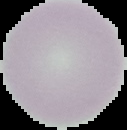

{
  "preparation": "thin blood film",
  "image_size": "127×130 pixels",
  "malaria_status": "uninfected",
  "image_type": "cell region segmented out of the field of view; surrounding area masked to black"
}